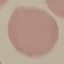
malaria status = uninfected
preparation = thin smear
stain = Giemsa
capture = smartphone through the microscope eyepiece
image type = cell patch, automatically extracted from a larger field of view and resized to 64 × 64 pixels